Assess this cell for malaria.
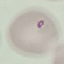

It is parasitized.

{
  "stain": "Giemsa",
  "capture": "smartphone camera at the microscope eyepiece",
  "preparation": "thin smear",
  "image_type": "cell patch, automatically extracted from a larger field of view and resized to 64 × 64 pixels"
}